Comment on the morphology of the erythrocytes.
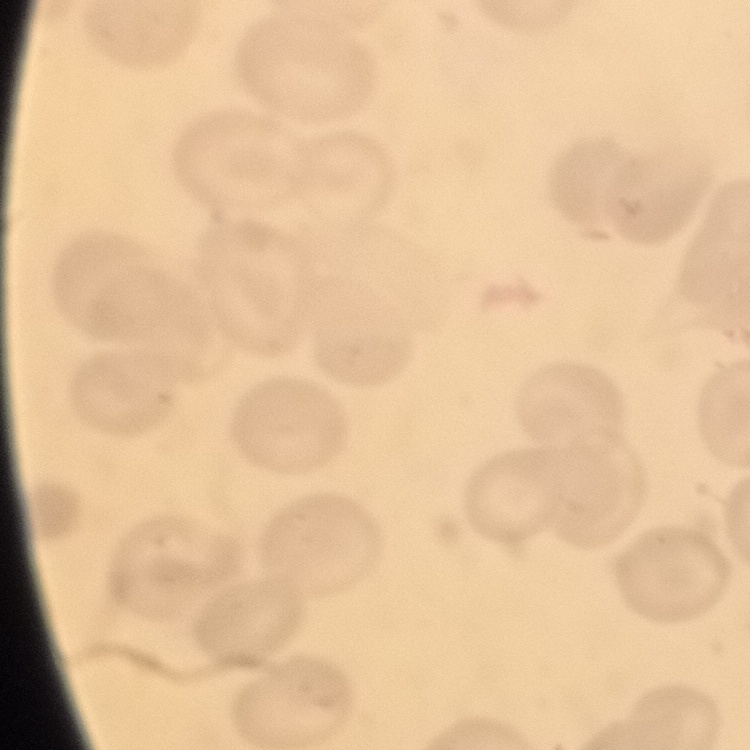

They show no rouleaux formation.

preparation = thin peripheral smear
stain = Field's or Giemsa
image type = square crop of a larger photomicrograph